Identify the parasite.
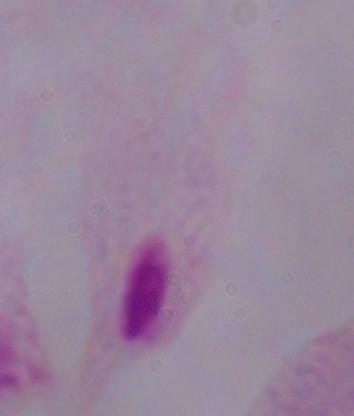
This is a trichomonad.

Summary:
  - Magnification: 1000x
  - Modality: micrograph